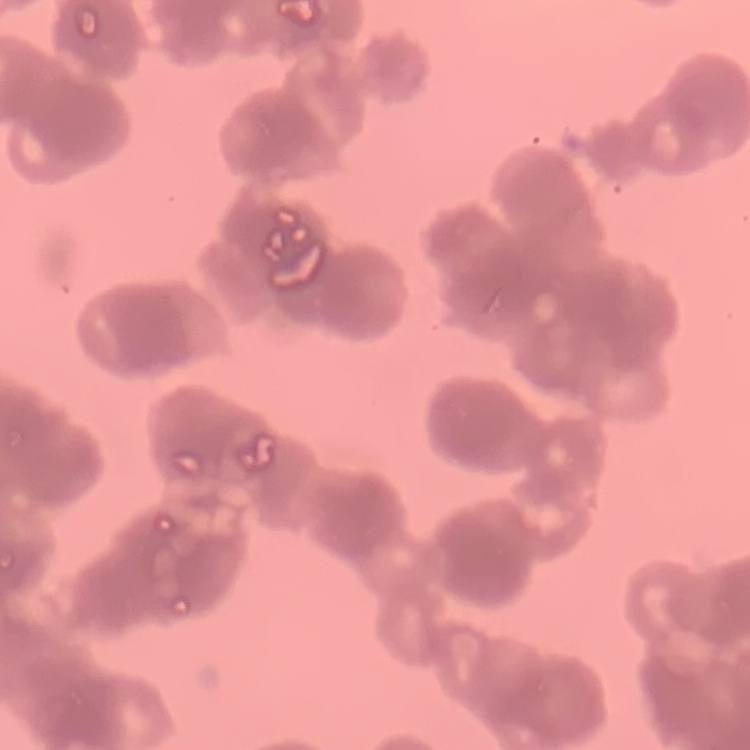
Summary:
  - Erythrocyte morphology: rouleaux formation
  - Preparation: thin peripheral smear
  - Stain: Field's or Giemsa
  - Image type: square crop of a larger photomicrograph